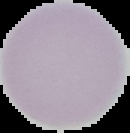

image_size: 130×133 pixels
preparation: thin blood film
result: no malaria parasites seen
image_type: segmented cell region with the area outside set to black